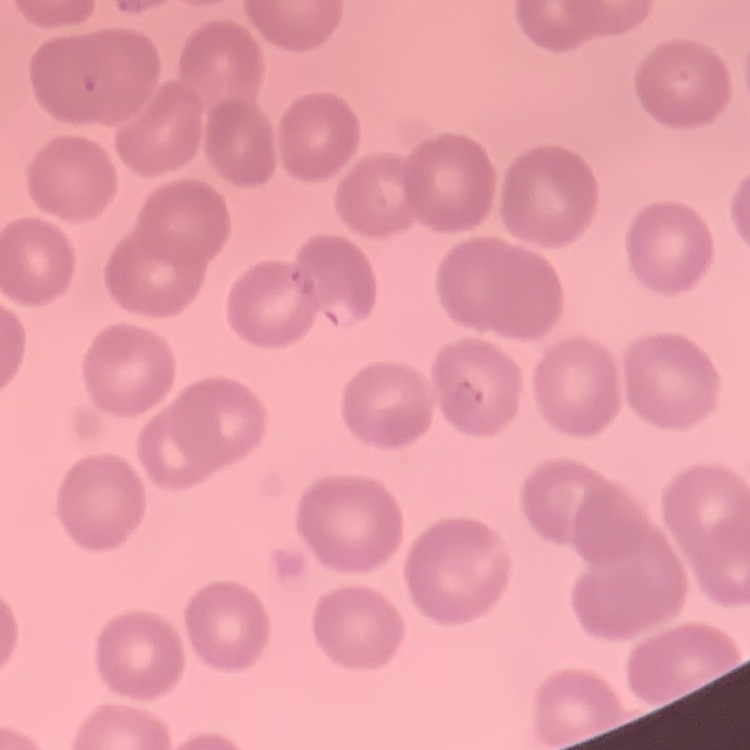
Summary:
  - Erythrocyte morphology: no rouleaux formation
  - Preparation: thin blood film
  - Image type: square crop of a larger photomicrograph
  - Stain: Field's or Giemsa